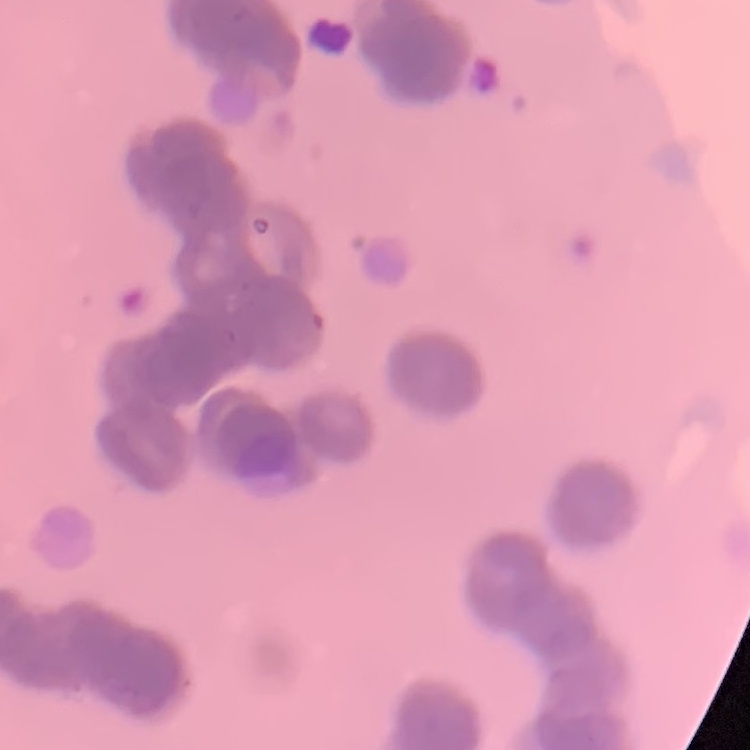

erythrocyte morphology = rouleaux formation
image type = one tile cut from a larger photomicrograph
stain = Field's or Giemsa
preparation = thin peripheral smear